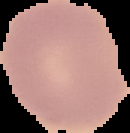

Summary:
  - Preparation: thin blood smear
  - Image size: 130×133 pixels
  - Image type: segmented cell region on a black background
  - Result: no malaria parasites seen